Identify the parasite.
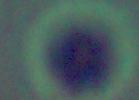

This is Leishmania.

magnification = 1000x
modality = micrograph